Report the malaria status of this cell.
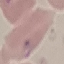

Parasitized.

image type = cell patch, automatically extracted from a larger field of view and resized to 64 × 64 pixels
capture = smartphone camera at the microscope eyepiece
preparation = thin blood smear
stain = Giemsa